Assess this cell for malaria.
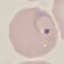
Parasitized.

Giemsa-stained preparation. Automatically extracted cell patch, resized to 64 × 64 pixels. Acquired by smartphone through the microscope eyepiece. Thin blood smear.